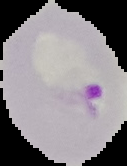
Result: malaria parasites detected. The area outside the segmented cell region is set to black. Image is 127×166 pixels. From a thin blood film.